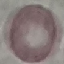
Result: no malaria parasites seen. Photographed with a smartphone camera at the microscope eyepiece. Giemsa stain. Thin blood film. Automatically extracted cell patch, resized to 64 × 64 pixels.